Report the malaria status of this cell.
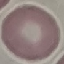
Uninfected.

Summary:
  - Stain: Giemsa
  - Capture: smartphone through the microscope eyepiece
  - Image type: automatically extracted cell patch, resized to 64 × 64 pixels
  - Preparation: thin blood smear